State the preparation type.
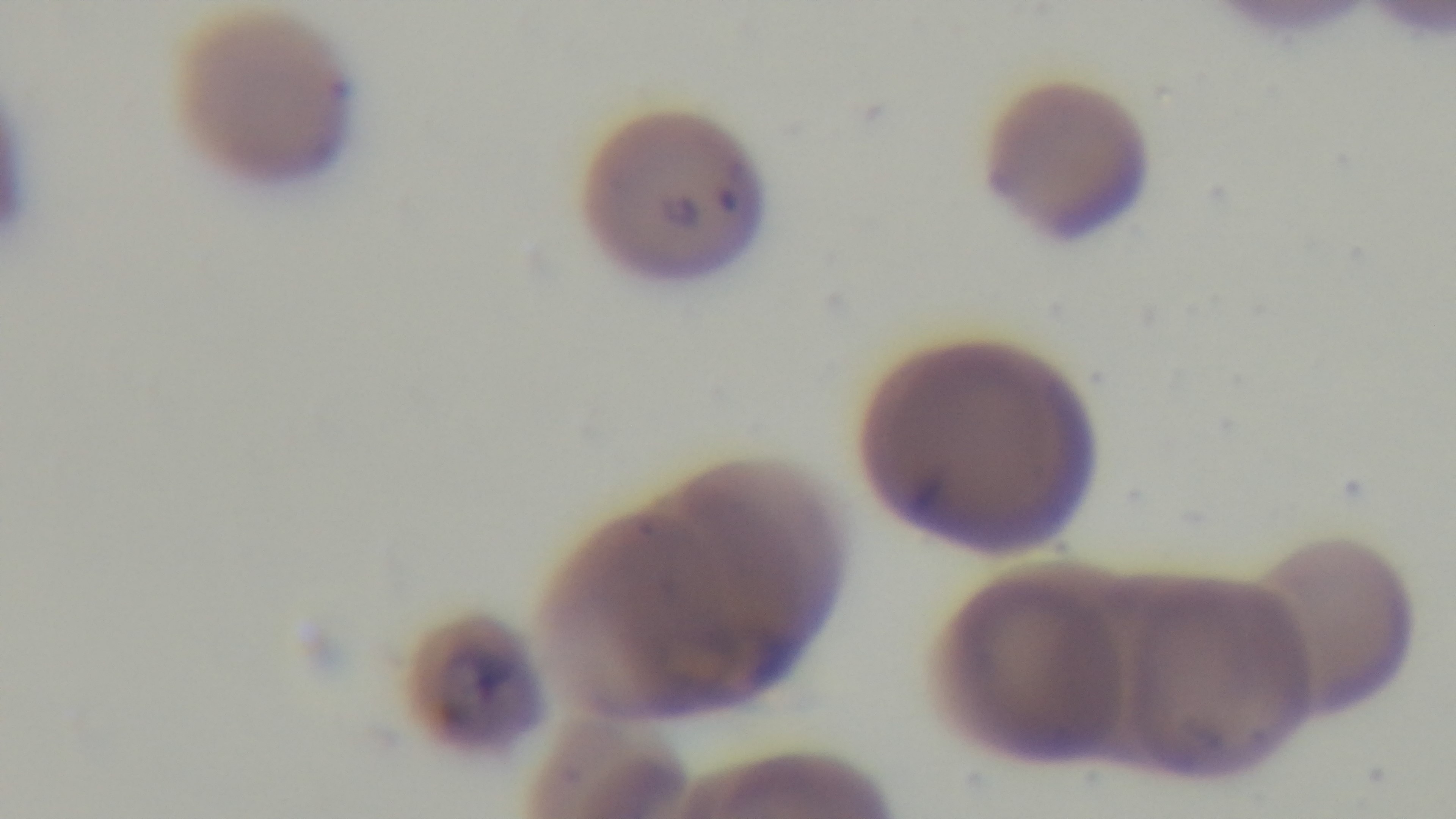
A thin smear.

Photomicrograph. Mounted 4K digital camera. Single field of view. Malaria status: infected. Oil-immersion objective, 100x. Giemsa-stained.